Locate platelets.
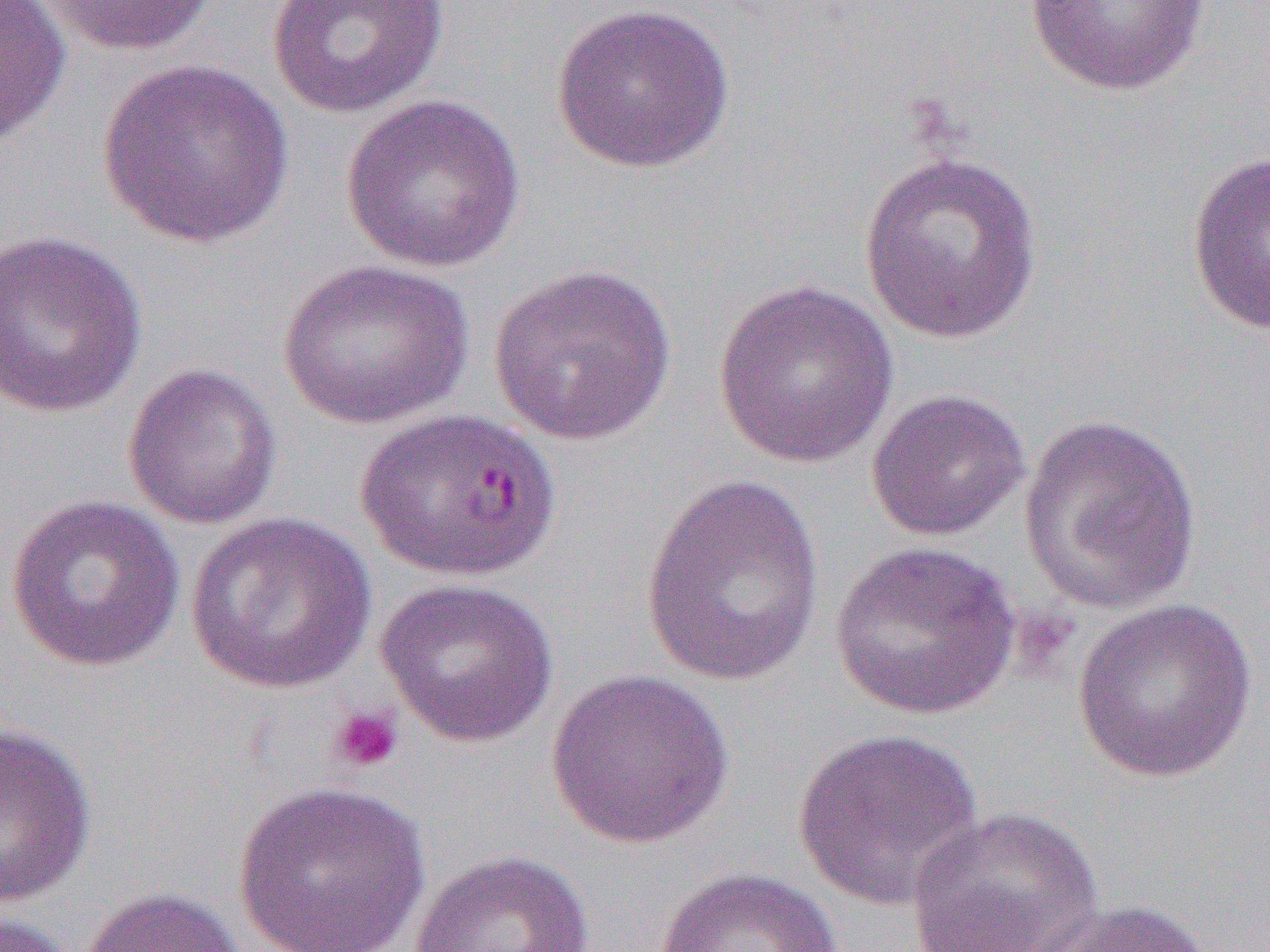
Approximate bounding boxes as (x1,y1)-(x2,y2) corner pairs in pixels.
Platelets: (1011,607)-(1079,675), (328,703)-(405,774).

Uninfected red blood cell locations: (1,0)-(71,148), (35,0)-(221,57), (265,1)-(451,119), (1024,1)-(1212,97), (550,2)-(736,175), (98,58)-(295,249), (340,92)-(527,273), (857,149)-(1045,346), (1186,150)-(1270,337), (0,230)-(148,419), (277,259)-(474,430), (486,263)-(678,447), (712,280)-(899,469), (122,362)-(282,531), (865,388)-(1031,542), (351,409)-(559,584), (1018,413)-(1203,615), (639,473)-(829,690), (5,493)-(185,673), (184,512)-(377,696), (830,540)-(1021,720), (375,576)-(559,747), (1071,597)-(1258,784), (546,668)-(734,849), (0,719)-(97,909), (791,726)-(984,910), (233,780)-(431,951), (906,806)-(1104,952), (408,849)-(596,952), (651,865)-(847,952), (78,885)-(245,952), (1036,897)-(1215,952), (0,910)-(79,952). Slide-level diagnosis: Plasmodium falciparum. One field of a larger specimen. Light microscopy. Thin blood film. 1000x magnification. Image is 1270×952 pixels.